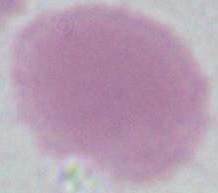 Captured at 1000x magnification. An erythrocyte is seen. Photomicrograph.